Describe the morphology of the red blood cells.
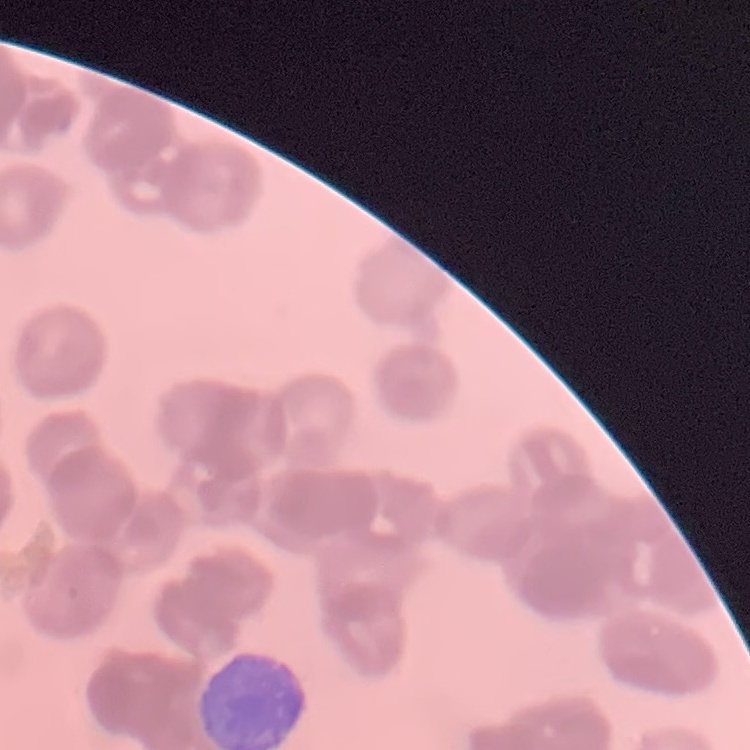
They show rouleaux formation.

Stained with either Field's or Giemsa. Square crop of a larger photomicrograph. Thin peripheral smear.